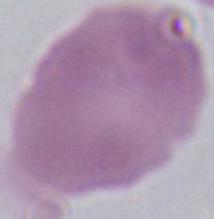
A red blood cell is shown. Micrograph. Captured at 1000x magnification.